Give the preparation type.
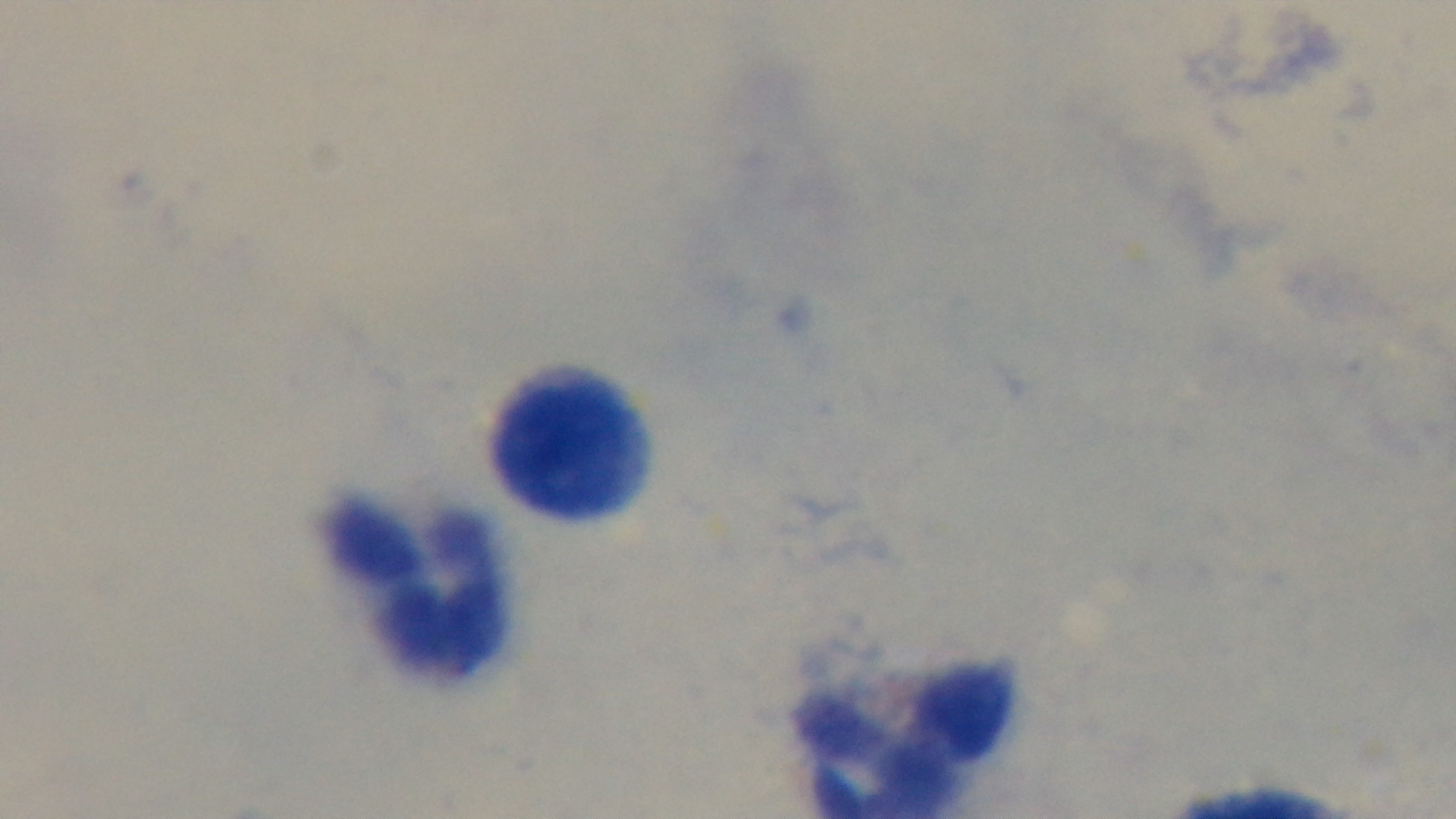
Thick.

Summary:
  - Field of view: single
  - Malaria status: negative
  - Stain: Giemsa
  - Objective: 100x oil immersion
  - Modality: light microscopy
  - Capture: mounted 4K digital camera